Comment on the morphology of the erythrocytes.
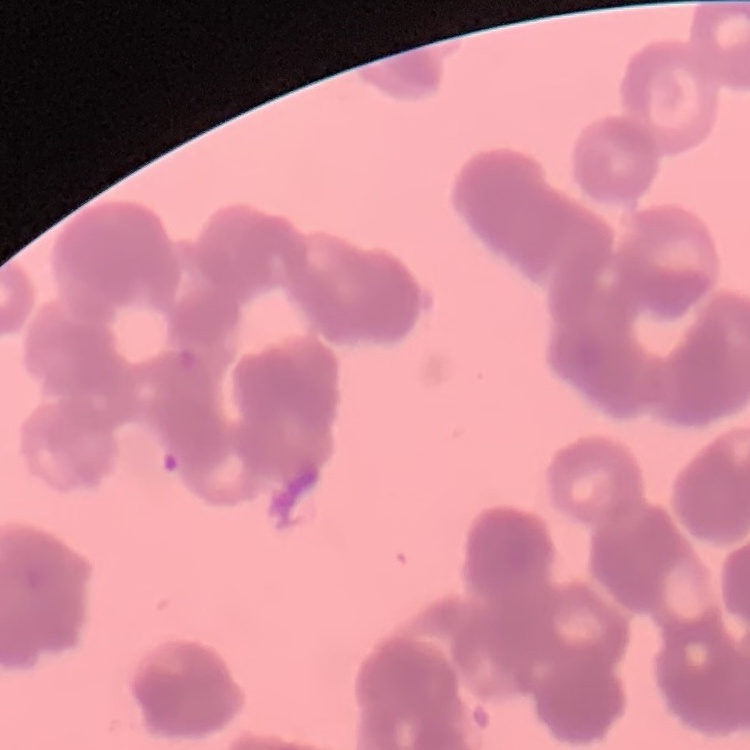
Rouleaux formation.

Square crop of a larger photomicrograph. Thin blood film. Stained with either Field's or Giemsa.